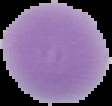

Malaria status: uninfected. The area outside the segmented cell region is set to black. Image is 112×106 pixels. From a thin blood film.